Name the parasite shown.
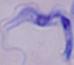
This is a trypanosome.

magnification: 1000x
modality: micrograph